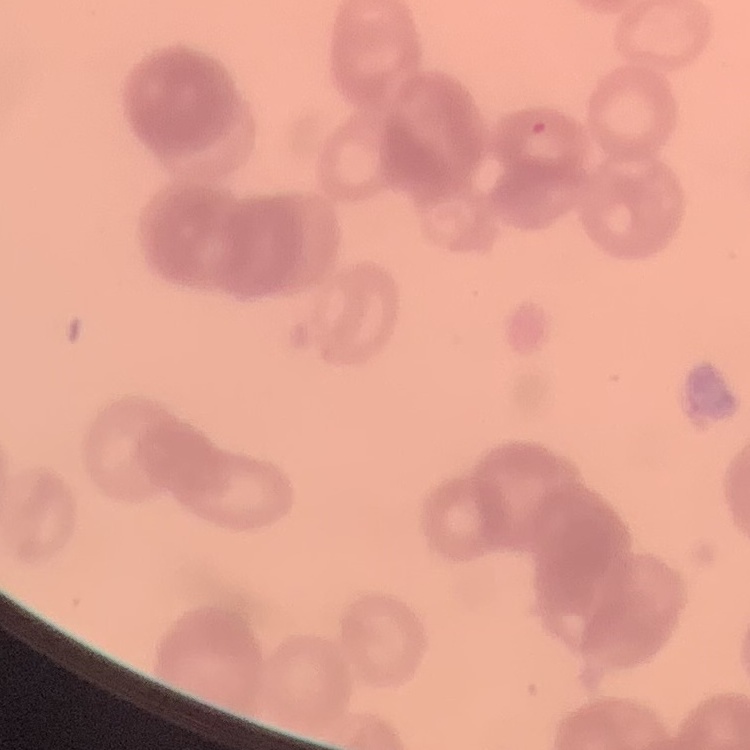 The red blood cells exhibit rouleaux formation. Square crop of a larger photomicrograph. Field's or Giemsa stain. Thin blood smear.